Assess this cell for malaria.
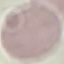

Uninfected.

Acquired by smartphone through the microscope eyepiece. Automatically extracted cell patch, resized to 64 × 64 pixels. Giemsa-stained preparation. Thin blood film.